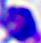

Summary:
  - Modality: photomicrograph
  - Identification: white blood cell
  - Magnification: 400x